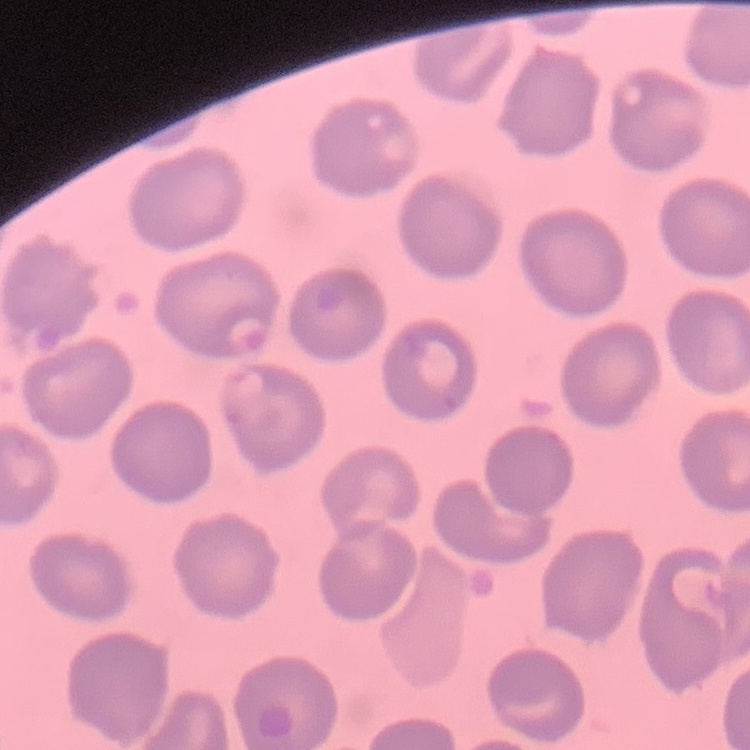
red blood cell morphology = no rouleaux formation
preparation = thin blood film
stain = Field's or Giemsa
image type = one tile cut from a larger photomicrograph